Name the parasite shown.
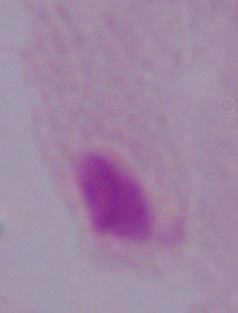
This is a trichomonad.

Micrograph. Captured at 1000x magnification.